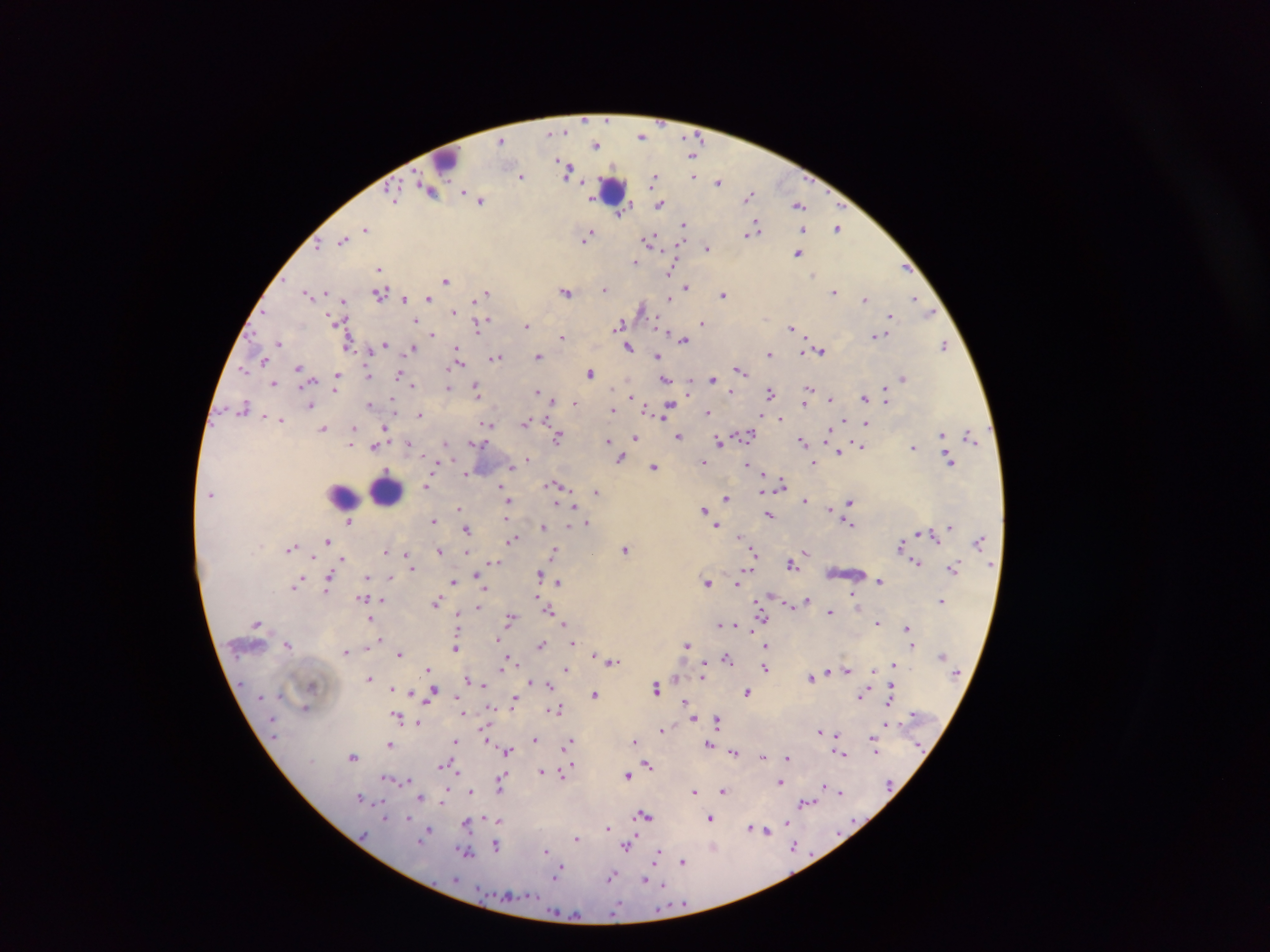
image size = 1270×952 pixels
leukocyte locations = approximate centers as [x, y] in pixels: [446, 159], [612, 188], [386, 490], [342, 494]
malaria parasite locations = approximate centers as [x, y] in pixels: [641, 136], [503, 140], [596, 145], [694, 155], [567, 169], [522, 175], [694, 176], [655, 179], [718, 182], [430, 190], [749, 195], [394, 196], [592, 197], [480, 199], [661, 204], [799, 205], [622, 212], [685, 226], [839, 227], [366, 228], [803, 229], [753, 232], [589, 235], [343, 239], [584, 239], [651, 241], [708, 249], [799, 253], [636, 262], [379, 267], [906, 267], [672, 270], [814, 273], [447, 279], [686, 286], [605, 287], [567, 291], [326, 292], [834, 292], [310, 293], [381, 293], [487, 293], [724, 294], [671, 296], [429, 298], [865, 298], [915, 298], [345, 299], [404, 299], [478, 299], [642, 308], [454, 311], [930, 312], [890, 314], [336, 319], [417, 320], [702, 322], [620, 324], [478, 325], [527, 326], [791, 328], [433, 334], [877, 334], [562, 336], [684, 338], [280, 343], [385, 344], [944, 344], [347, 345], [413, 347], [629, 347], [458, 348], [821, 350], [369, 351], [804, 351], [769, 352], [657, 355], [538, 356], [496, 357], [460, 359], [264, 361], [244, 369], [299, 369], [740, 370], [591, 372], [400, 373], [368, 374], [338, 376], [712, 378], [903, 378], [665, 379], [275, 382], [689, 382], [413, 384], [448, 387], [809, 387], [336, 389], [476, 389], [537, 392], [770, 392], [732, 393], [886, 394], [631, 396], [865, 397], [394, 399], [830, 399], [553, 400], [886, 400], [575, 402], [806, 402], [311, 404], [370, 404], [670, 406], [243, 407], [648, 408], [613, 409], [708, 412], [667, 413], [419, 415], [662, 416], [267, 418], [780, 418], [281, 419], [844, 419], [526, 421], [486, 423], [866, 424], [385, 426], [323, 428], [354, 428], [829, 430], [942, 432], [747, 434], [559, 436], [679, 436], [970, 436], [353, 437], [636, 437], [608, 439], [806, 439], [719, 441], [408, 442], [446, 442], [476, 442], [803, 442], [351, 445], [375, 445], [861, 445], [914, 447], [838, 452], [620, 457], [528, 459], [950, 459], [703, 462], [749, 463], [814, 463], [512, 465], [653, 466], [436, 468], [764, 473], [467, 474], [782, 485], [427, 486], [556, 486], [503, 489], [762, 490], [596, 492], [506, 493], [726, 497], [509, 500], [806, 501], [850, 502], [573, 506], [459, 509], [704, 509], [829, 509], [769, 514], [506, 518], [433, 519], [351, 521], [849, 521], [587, 522], [569, 524], [544, 526], [718, 527], [949, 528], [467, 529], [919, 534], [933, 534], [740, 535], [745, 537], [513, 538], [329, 540], [979, 541], [901, 545], [291, 547], [625, 548], [439, 550], [386, 551], [753, 551], [466, 552], [555, 552], [592, 552], [806, 552], [407, 553], [343, 558], [494, 561], [916, 562], [792, 563], [411, 566], [954, 568], [748, 569], [541, 574], [368, 575], [391, 576], [329, 579], [301, 580], [454, 581], [879, 581], [559, 582], [708, 582], [737, 583], [297, 585], [487, 588], [327, 591], [853, 597], [363, 598], [537, 598], [808, 599], [382, 600], [942, 600], [438, 601], [760, 601], [786, 602], [858, 603], [478, 606], [549, 608], [831, 611], [458, 614], [761, 615], [510, 617], [370, 618], [878, 621], [258, 622], [720, 622], [565, 624], [736, 624], [908, 628], [497, 638], [381, 639], [573, 643], [288, 644], [541, 644], [687, 644], [371, 645], [766, 646], [912, 646], [456, 647], [345, 651], [399, 652], [595, 654], [728, 657], [507, 658], [612, 661], [894, 664], [703, 665], [503, 666], [765, 667], [566, 668], [428, 669], [828, 669], [847, 669], [874, 670], [812, 676], [369, 677], [703, 677], [467, 678], [677, 678], [529, 681], [484, 684], [550, 685], [657, 687], [392, 688], [891, 689], [396, 690], [747, 691], [432, 692], [595, 694], [863, 694], [458, 696], [514, 699], [687, 700], [889, 703], [306, 707], [490, 707], [556, 708], [463, 712], [914, 713], [398, 715], [693, 719], [717, 719], [417, 723], [887, 725], [662, 729], [487, 731], [820, 731], [839, 734], [872, 738], [535, 739], [635, 740], [455, 741], [487, 741], [570, 742], [390, 743], [709, 744], [568, 745], [876, 748], [507, 750], [734, 750], [839, 752], [353, 756], [763, 756], [788, 757], [443, 765], [649, 766], [570, 767], [457, 770], [542, 771], [563, 772], [503, 774], [628, 775], [389, 778], [406, 779], [502, 779], [781, 781], [472, 789], [501, 789], [824, 789], [694, 790], [724, 790], [839, 791], [448, 792], [360, 797], [421, 798], [808, 802], [383, 804], [646, 815], [385, 816], [409, 818], [711, 818], [497, 821], [788, 821], [468, 822], [751, 827], [607, 828], [429, 830], [765, 830], [577, 837], [421, 838], [497, 845], [627, 845], [794, 846], [465, 850], [545, 851], [657, 856], [683, 861], [559, 869], [612, 876], [646, 880], [663, 884]
field of view = single
country = Ghana
capture = mobile-phone photograph through a microscope
preparation = thick blood film